Classify this cell by malaria status.
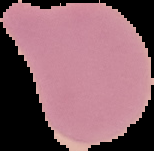

Uninfected.

Summary:
  - Image type: cell region segmented out of the field of view; surrounding area masked to black
  - Preparation: thin blood smear
  - Image size: 154×151 pixels